Identify the parasite.
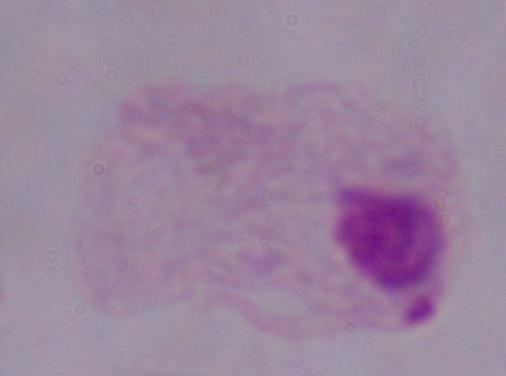

A trichomonad.

modality = photomicrograph
magnification = 1000x